Locate and identify every blood parasite.
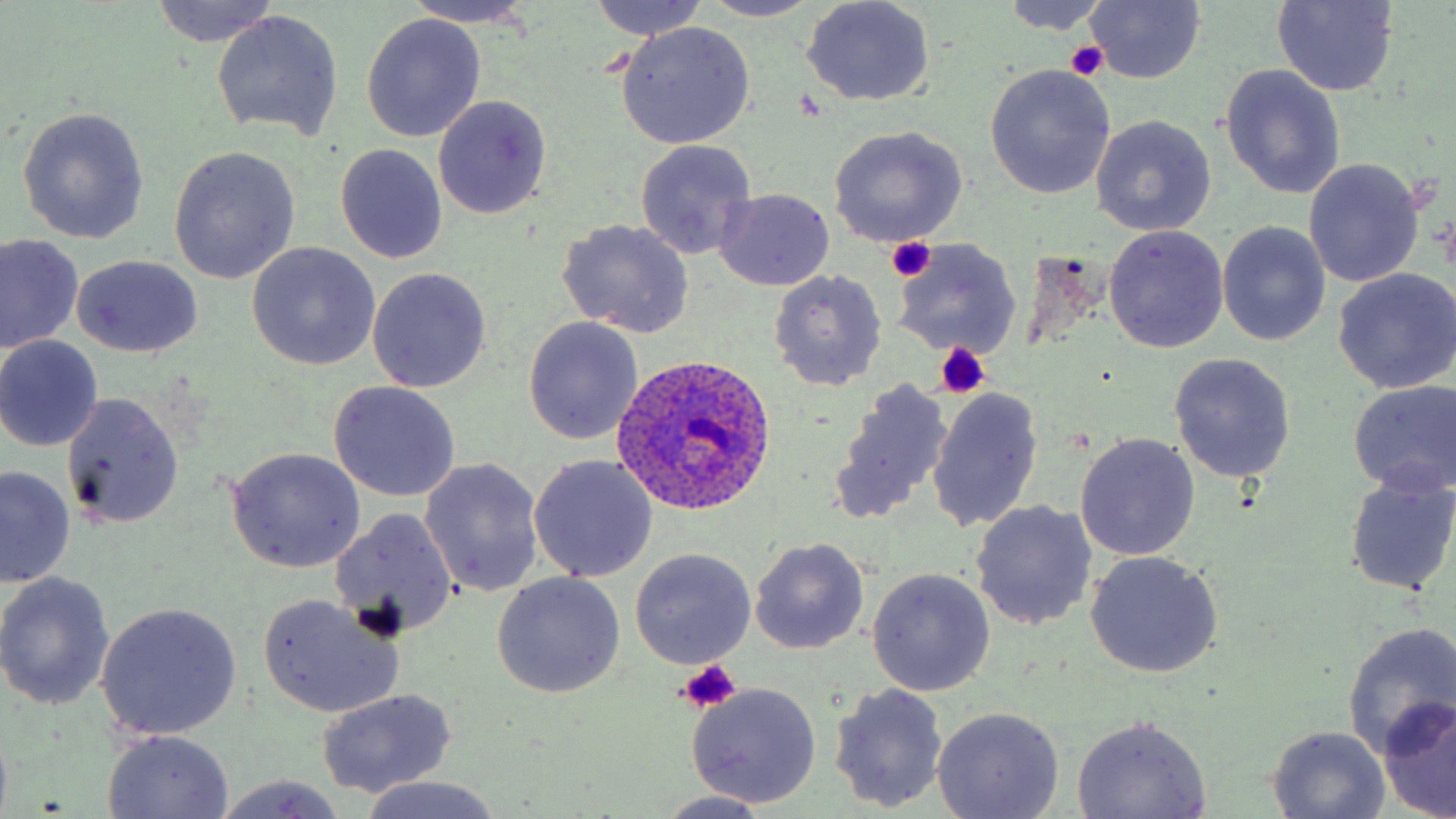

Approximate bounding boxes as (x1,y1)-(x2,y2) corner pairs in pixels.
Plasmodium ovale-infected red blood cells: (611,354)-(778,516).
No Plasmodium falciparum, Plasmodium malariae, Plasmodium vivax, Babesia divergens, or Trypanosoma brucei observed.

slide-level diagnosis = Plasmodium ovale
uninfected red blood cell locations = approximate bounding boxes as (x1,y1)-(x2,y2) corner pairs in pixels: (150,0)-(280,48), (589,0)-(707,42), (698,0)-(827,22), (405,1)-(539,28), (801,1)-(935,107), (999,1)-(1114,33), (1084,1)-(1206,83), (1272,1)-(1399,95), (212,10)-(344,143), (361,14)-(486,143), (615,21)-(756,149), (984,64)-(1116,199), (1220,65)-(1347,200), (433,94)-(552,218), (16,109)-(149,246), (1090,117)-(1217,237), (826,125)-(968,248), (634,140)-(758,260), (334,143)-(447,264), (168,145)-(300,285), (1303,159)-(1425,288), (715,189)-(835,291), (557,218)-(695,339), (1219,221)-(1331,347), (1104,225)-(1229,352), (2,235)-(83,354), (893,238)-(1020,361), (247,243)-(381,370), (73,256)-(203,358), (366,267)-(492,393), (1332,268)-(1456,394), (768,270)-(886,392), (523,317)-(643,445), (0,335)-(104,451), (1167,353)-(1295,484), (830,378)-(954,523), (327,380)-(461,502), (1346,380)-(1456,496), (926,385)-(1044,533), (61,391)-(184,530), (1074,433)-(1200,560), (227,448)-(365,573), (528,455)-(659,583), (420,458)-(546,599), (1,467)-(75,586), (1343,473)-(1456,597), (971,500)-(1098,632), (329,509)-(458,638), (748,537)-(870,655), (629,548)-(756,669), (1085,552)-(1223,678), (866,568)-(995,697), (0,572)-(115,710), (490,572)-(626,699), (256,595)-(404,718), (97,602)-(242,741), (1341,622)-(1456,759), (683,682)-(823,808), (829,683)-(950,813), (315,690)-(457,798), (1378,696)-(1456,818), (932,706)-(1065,819), (1071,715)-(1213,818), (1267,727)-(1391,816), (103,731)-(233,817), (212,774)-(350,817), (355,776)-(505,818), (653,792)-(776,818)
stain = May-Grünwald-Giemsa
modality = light microscopy
platelet locations = approximate bounding boxes as (x1,y1)-(x2,y2) corner pairs in pixels: (1065,41)-(1107,81), (885,237)-(938,282), (933,344)-(989,398), (677,658)-(745,713)
preparation = thin blood smear
magnification = 1000x
field of view = single
image size = 1456×819 pixels